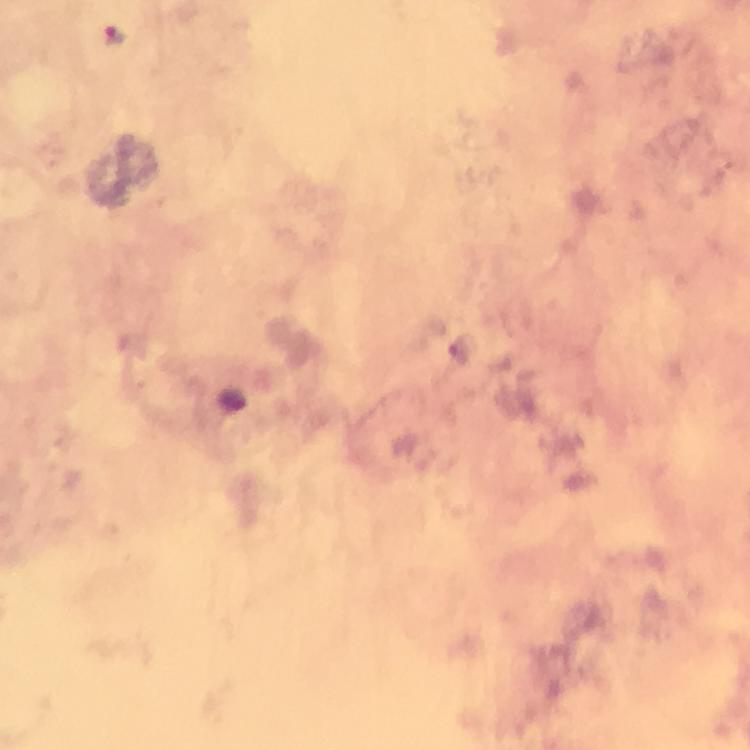
Approximate object centers, in pixels from the top-left corner. Plasmodium parasite locations: (x=113, y=34). Giemsa-stained preparation. Cropped region of a single field of view. Smartphone photograph taken through a microscope. Thick smear. At 100x magnification. Immersion oil was used. From a malaria diagnostic workup. Image is 750×750 pixels.